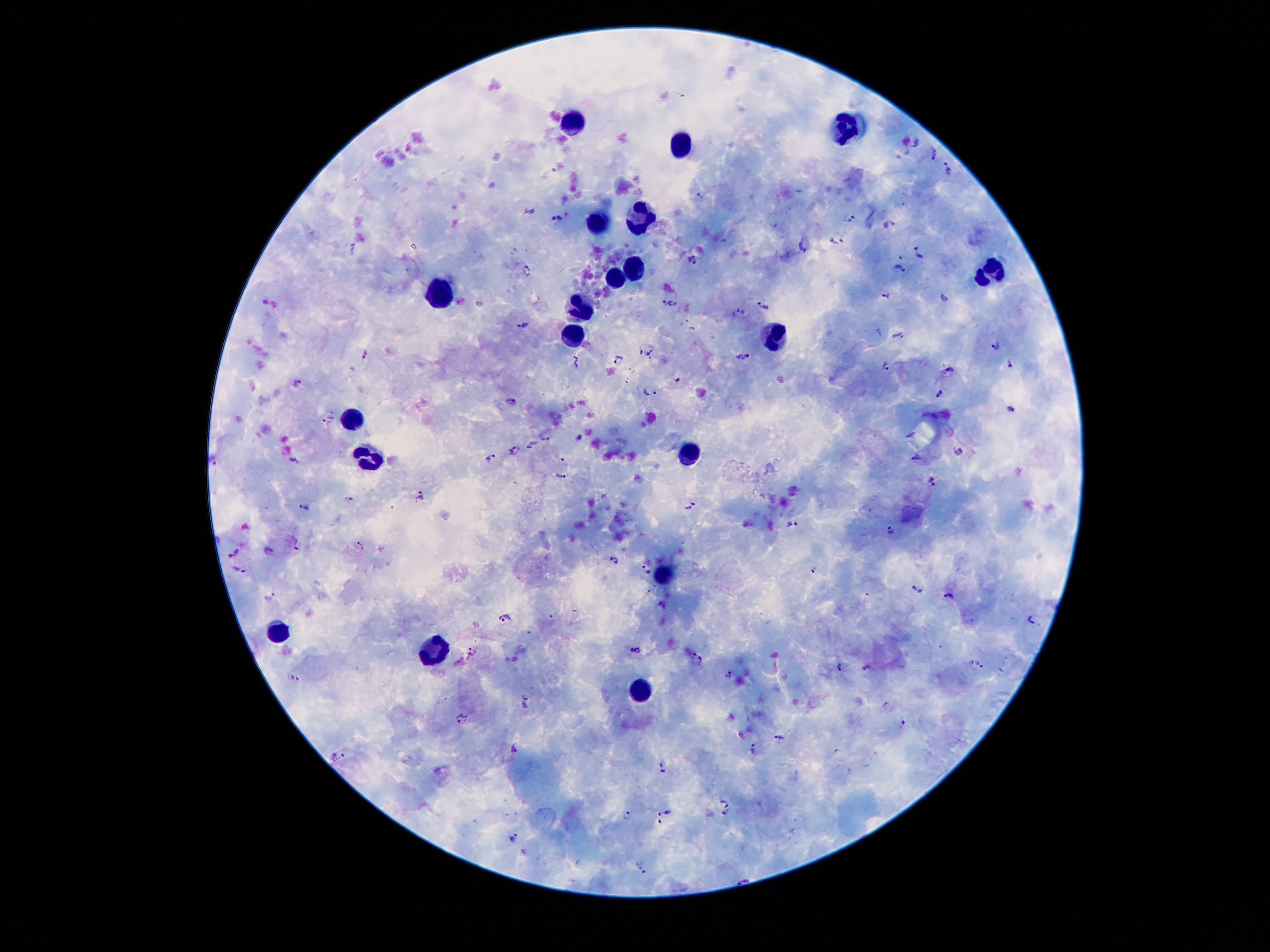 Approximate centers as (x, y) in pixels. Plasmodium parasite locations: (915, 142), (935, 156), (948, 171), (700, 196), (530, 213), (557, 217), (851, 217), (889, 224), (837, 238), (803, 245), (353, 248), (919, 255), (692, 260), (527, 269), (901, 269), (944, 296), (887, 297), (670, 302), (764, 306), (739, 312), (522, 325), (692, 329), (899, 335), (996, 345), (647, 350), (365, 354), (743, 356), (619, 359), (575, 363), (1010, 363), (885, 365), (950, 369), (677, 381), (297, 383), (649, 390), (939, 391), (512, 401), (1010, 408), (328, 418), (581, 436), (546, 438), (515, 450), (960, 451), (492, 457), (213, 458), (917, 458), (563, 459), (294, 461), (562, 477), (932, 483), (420, 495), (350, 498), (694, 502), (305, 507), (793, 524), (889, 530), (296, 544), (362, 544), (269, 551), (233, 553), (614, 559), (815, 568), (240, 569), (647, 569), (917, 588), (271, 596), (946, 596), (506, 619), (1031, 620), (472, 650), (636, 650), (699, 658), (841, 665), (980, 666), (866, 668), (728, 673), (296, 677), (526, 703), (463, 720), (902, 724), (779, 737), (513, 749), (754, 749), (338, 757), (664, 765), (724, 804), (666, 811), (629, 814), (725, 814), (514, 839), (641, 869). Leukocyte locations: (849, 122), (569, 123), (679, 142), (599, 221), (640, 222), (635, 266), (990, 275), (616, 282), (438, 298), (579, 308), (776, 335), (575, 339), (351, 419), (693, 455), (367, 459), (663, 577), (278, 637), (431, 652), (641, 698). Image is 1270×952 pixels. Smartphone photograph taken through the microscope eyepiece. Patient malaria status: positive for Plasmodium falciparum. 100x magnification. Thick peripheral-blood smear. One field from this slide. Giemsa stain.